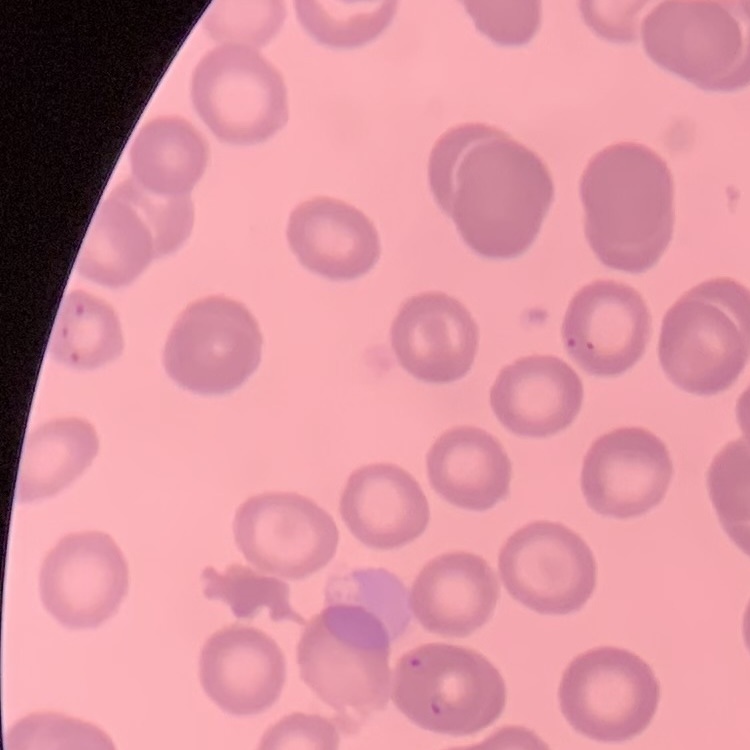
Summary:
  - Red blood cell morphology: no rouleaux formation
  - Stain: Field's or Giemsa
  - Image type: square crop of a larger photomicrograph
  - Preparation: thin blood smear